Give the extent of all Plasmodium malariae-infected red blood cells.
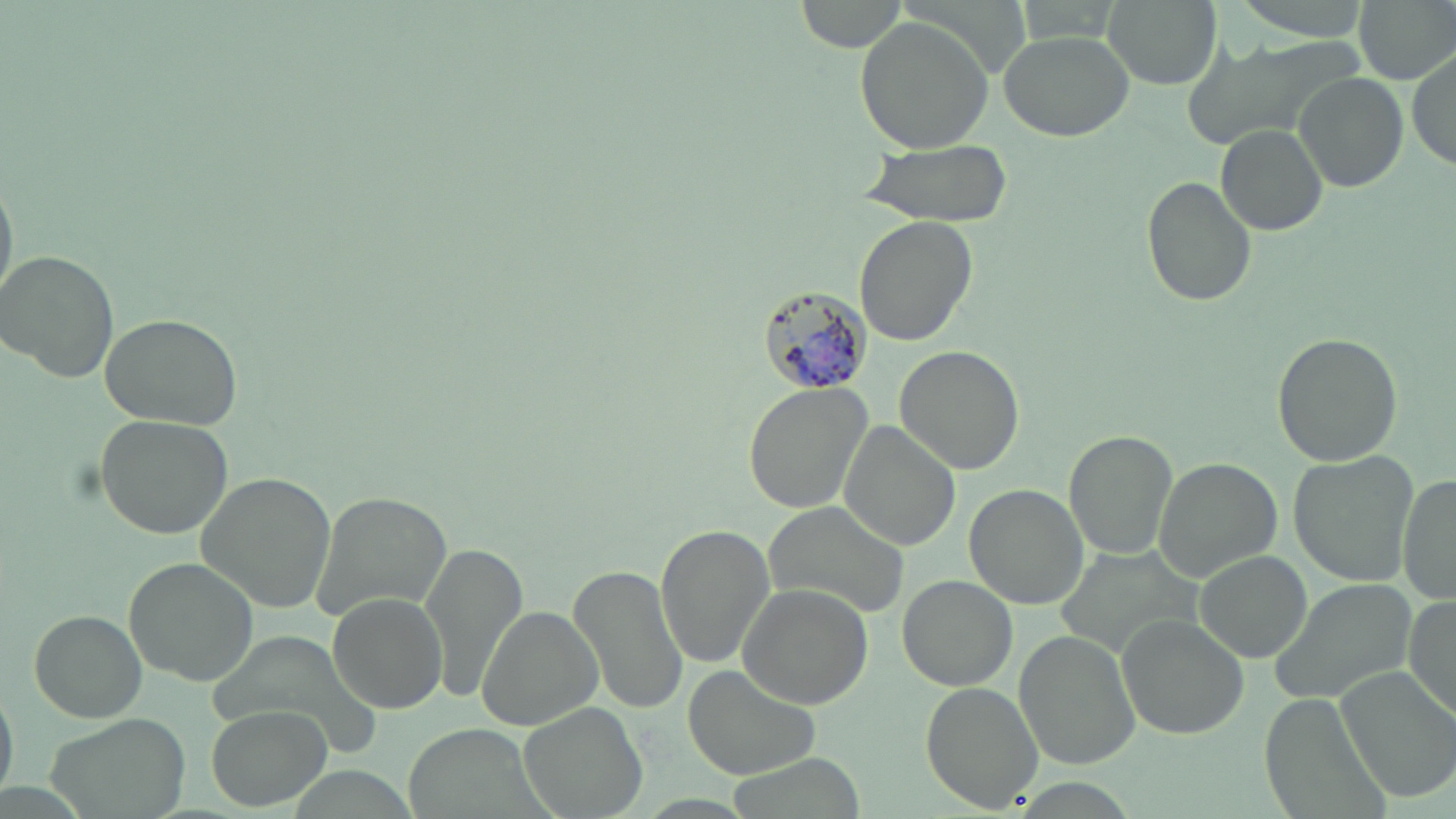

Approximate bounding boxes as named x1/y1/x2/y2 corners in pixels.
Plasmodium malariae-infected red blood cells: (x1=751, y1=285, x2=869, y2=399).

Summary:
  - Uninfected red blood cell locations: (x1=793, y1=0, x2=909, y2=54), (x1=1103, y1=0, x2=1220, y2=89), (x1=1228, y1=0, x2=1375, y2=38), (x1=1352, y1=0, x2=1456, y2=83), (x1=853, y1=17, x2=991, y2=154), (x1=998, y1=29, x2=1133, y2=140), (x1=1412, y1=48, x2=1454, y2=174), (x1=1296, y1=73, x2=1409, y2=192), (x1=1215, y1=124, x2=1329, y2=236), (x1=853, y1=140, x2=1016, y2=225), (x1=0, y1=170, x2=17, y2=311), (x1=1143, y1=175, x2=1257, y2=307), (x1=856, y1=214, x2=979, y2=347), (x1=0, y1=249, x2=119, y2=380), (x1=99, y1=312, x2=244, y2=431), (x1=1273, y1=332, x2=1401, y2=467), (x1=893, y1=344, x2=1025, y2=475), (x1=742, y1=381, x2=872, y2=514), (x1=95, y1=414, x2=235, y2=539), (x1=840, y1=421, x2=963, y2=551), (x1=1064, y1=431, x2=1175, y2=559), (x1=1290, y1=451, x2=1423, y2=584), (x1=1156, y1=457, x2=1282, y2=583), (x1=1398, y1=468, x2=1454, y2=606), (x1=193, y1=470, x2=336, y2=615), (x1=965, y1=484, x2=1088, y2=609), (x1=310, y1=489, x2=452, y2=625), (x1=766, y1=502, x2=911, y2=621), (x1=654, y1=525, x2=776, y2=669), (x1=419, y1=541, x2=528, y2=705), (x1=1194, y1=551, x2=1313, y2=664), (x1=122, y1=556, x2=259, y2=685), (x1=568, y1=565, x2=689, y2=715), (x1=899, y1=576, x2=1016, y2=691), (x1=1270, y1=578, x2=1413, y2=706), (x1=738, y1=583, x2=876, y2=710), (x1=330, y1=592, x2=445, y2=714), (x1=1400, y1=593, x2=1456, y2=722), (x1=476, y1=604, x2=602, y2=731), (x1=29, y1=610, x2=147, y2=724), (x1=1118, y1=617, x2=1248, y2=737), (x1=1014, y1=631, x2=1141, y2=770), (x1=684, y1=665, x2=822, y2=780), (x1=1335, y1=667, x2=1456, y2=802), (x1=921, y1=682, x2=1045, y2=812), (x1=0, y1=684, x2=18, y2=803), (x1=517, y1=702, x2=650, y2=819), (x1=205, y1=708, x2=330, y2=809), (x1=43, y1=710, x2=192, y2=819)
  - Slide-level diagnosis: Plasmodium malariae
  - Magnification: 1000x
  - Stain: May-Grünwald-Giemsa
  - Image size: 1456×819 pixels
  - Field of view: single
  - Preparation: thin blood smear
  - Modality: optical microscopy